Locate and identify every blood parasite.
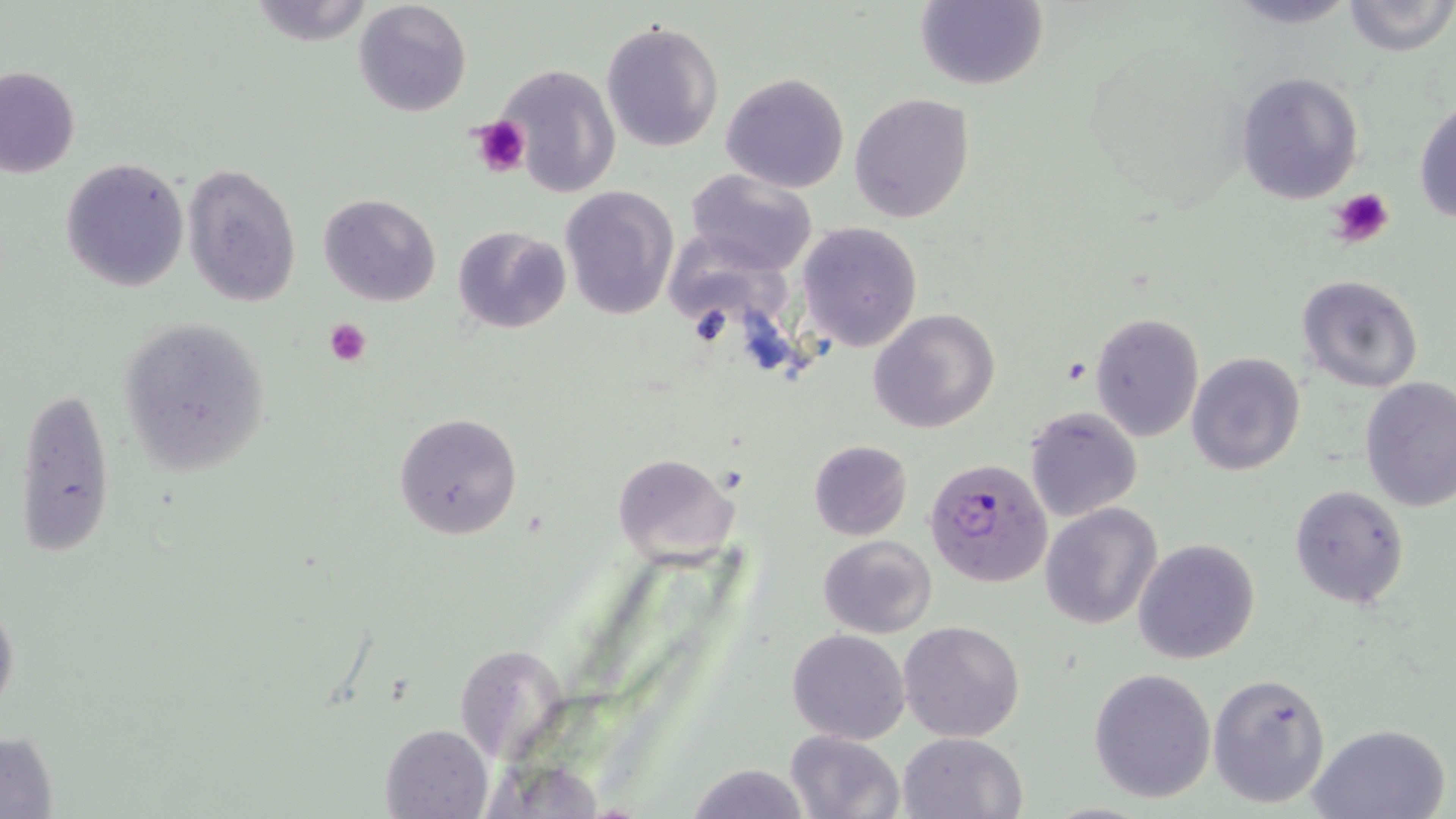

Approximate bounding boxes as named x1/y1/x2/y2 corners in pixels.
Plasmodium falciparum-infected red blood cells: (x1=923, y1=457, x2=1053, y2=588).
No Plasmodium ovale, Plasmodium malariae, Plasmodium vivax, Babesia divergens, or Trypanosoma brucei observed.

Platelet locations: (x1=469, y1=116, x2=529, y2=177), (x1=1329, y1=187, x2=1394, y2=247), (x1=324, y1=318, x2=372, y2=366). Uninfected red blood cell locations: (x1=915, y1=0, x2=1047, y2=91), (x1=1341, y1=0, x2=1455, y2=55), (x1=243, y1=1, x2=378, y2=45), (x1=352, y1=1, x2=471, y2=117), (x1=600, y1=19, x2=725, y2=153), (x1=497, y1=63, x2=620, y2=194), (x1=0, y1=65, x2=81, y2=178), (x1=1233, y1=70, x2=1366, y2=206), (x1=720, y1=72, x2=850, y2=193), (x1=849, y1=93, x2=975, y2=223), (x1=1414, y1=95, x2=1456, y2=225), (x1=60, y1=158, x2=189, y2=292), (x1=181, y1=162, x2=302, y2=306), (x1=684, y1=167, x2=820, y2=276), (x1=560, y1=185, x2=678, y2=323), (x1=318, y1=193, x2=440, y2=307), (x1=797, y1=222, x2=923, y2=353), (x1=452, y1=224, x2=572, y2=335), (x1=668, y1=245, x2=791, y2=327), (x1=1296, y1=275, x2=1423, y2=393), (x1=869, y1=308, x2=1001, y2=434), (x1=1091, y1=312, x2=1204, y2=441), (x1=117, y1=315, x2=274, y2=476), (x1=1186, y1=352, x2=1306, y2=477), (x1=1358, y1=377, x2=1456, y2=512), (x1=13, y1=386, x2=116, y2=561), (x1=1024, y1=405, x2=1144, y2=521), (x1=393, y1=411, x2=523, y2=541), (x1=807, y1=439, x2=913, y2=540), (x1=614, y1=453, x2=739, y2=570), (x1=1288, y1=483, x2=1411, y2=610), (x1=1039, y1=502, x2=1162, y2=629), (x1=818, y1=534, x2=937, y2=639), (x1=1132, y1=538, x2=1260, y2=665), (x1=0, y1=593, x2=19, y2=723), (x1=899, y1=620, x2=1025, y2=742), (x1=787, y1=629, x2=911, y2=744), (x1=1088, y1=668, x2=1217, y2=803), (x1=1208, y1=673, x2=1332, y2=809), (x1=379, y1=722, x2=494, y2=818), (x1=1305, y1=722, x2=1451, y2=819), (x1=1, y1=731, x2=59, y2=816), (x1=784, y1=731, x2=906, y2=819), (x1=898, y1=731, x2=1026, y2=818), (x1=683, y1=762, x2=811, y2=819). Slide-level diagnosis: Plasmodium falciparum. One field of a larger specimen. Thin blood smear. Captured at 1000x magnification. Optical microscopy. Image is 1456×819 pixels. May-Grünwald-Giemsa stain.